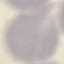 Result: no malaria parasites detected. Cell patch, automatically extracted from a larger field of view and resized to 64 × 64 pixels. Thin blood smear. Photographed with a smartphone camera at the microscope eyepiece. Giemsa stain.